Name the parasite shown.
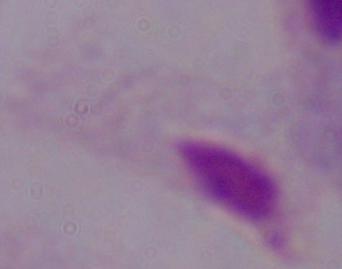
A trichomonad.

{
  "magnification": "1000x",
  "modality": "micrograph"
}